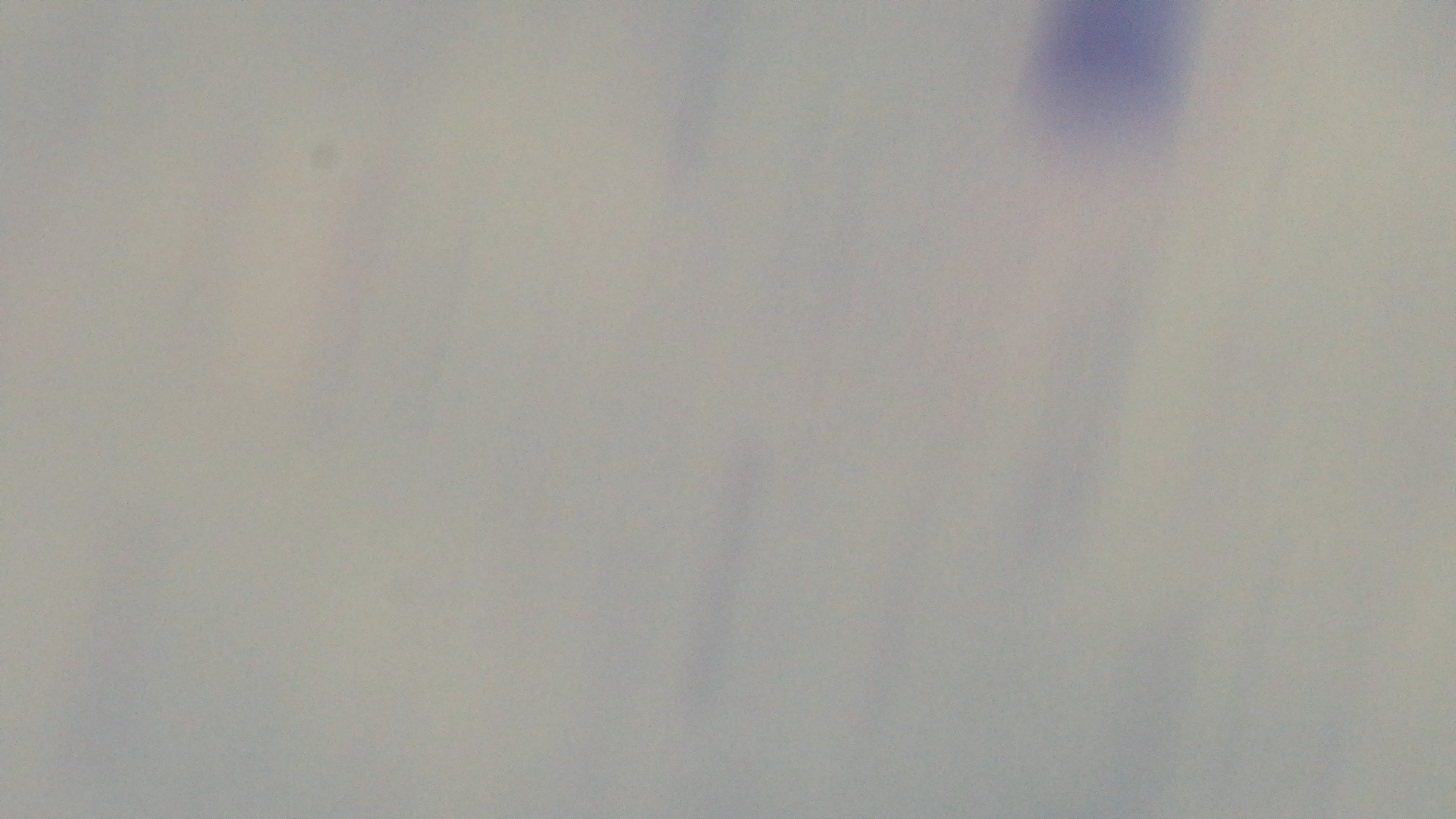

modality = light microscopy
capture = mounted 4K digital camera
malaria status = negative
preparation = thick blood film
field of view = single
stain = Giemsa
objective = 100x oil immersion